Identify the blood parasite species.
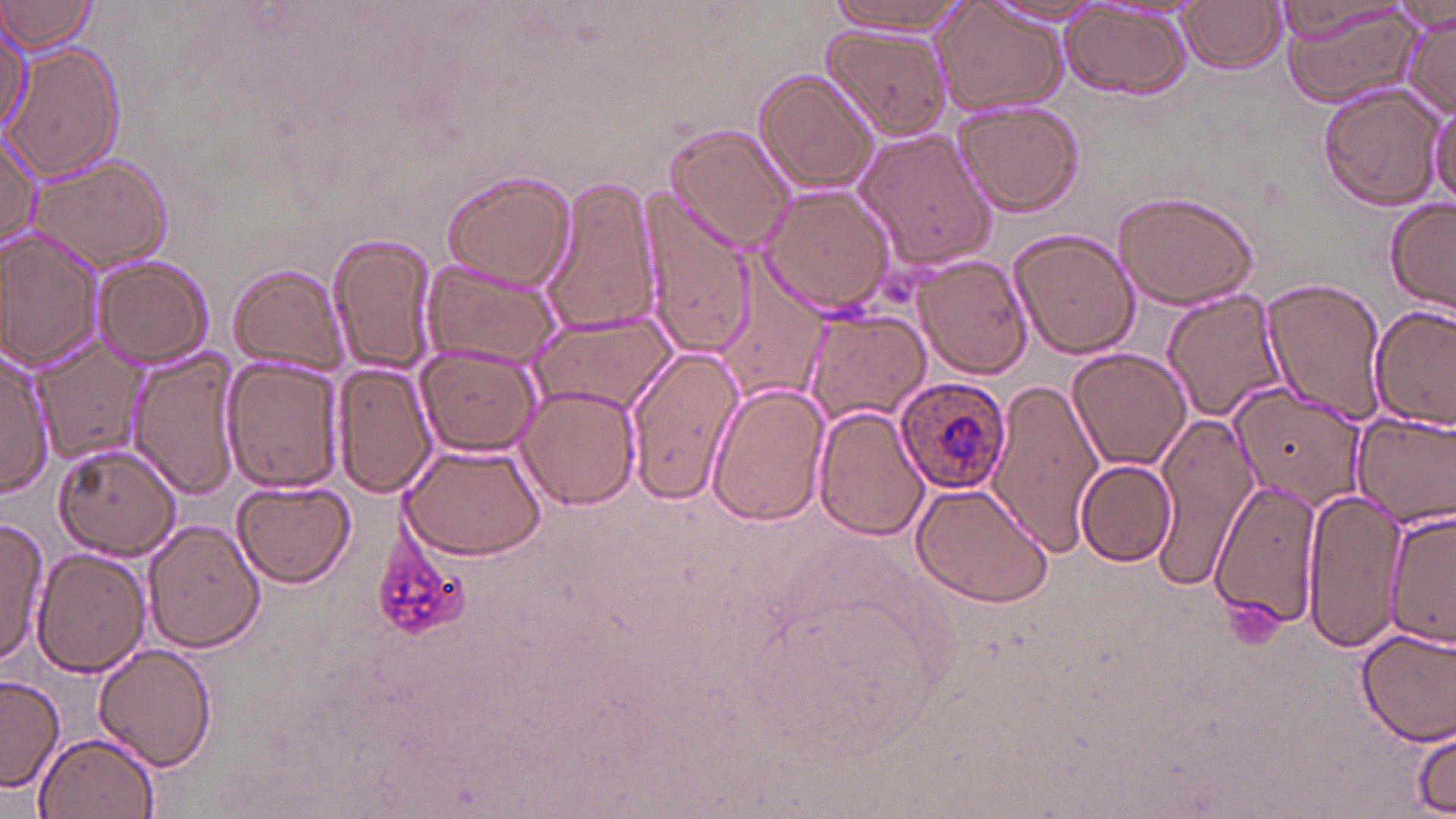

Plasmodium ovale.

magnification = 1000x
image size = 1456×819 pixels
stain = May-Grünwald-Giemsa
modality = optical microscopy
field of view = one of a larger specimen
Plasmodium ovale-infected red blood cell locations = approximate bounding boxes as [x1, y1, x2, y2] in pixels: [896, 375, 1011, 496]
platelet locations = approximate bounding boxes as [x1, y1, x2, y2] in pixels: [373, 520, 474, 642], [1225, 593, 1285, 649]
preparation = thin blood film
uninfected red blood cell locations = approximate bounding boxes as [x1, y1, x2, y2] in pixels: [0, 0, 102, 58], [828, 0, 974, 35], [983, 1, 1109, 28], [1179, 1, 1287, 73], [1278, 1, 1426, 112], [933, 3, 1069, 116], [1270, 3, 1417, 45], [1060, 5, 1193, 101], [1400, 9, 1455, 121], [0, 18, 28, 137], [826, 26, 950, 144], [8, 44, 124, 182], [753, 68, 878, 195], [1321, 84, 1445, 209], [1427, 91, 1454, 213], [952, 100, 1086, 217], [1, 122, 44, 252], [666, 123, 796, 250], [855, 129, 999, 272], [29, 153, 174, 273], [440, 168, 577, 292], [539, 174, 661, 335], [760, 185, 897, 316], [641, 188, 755, 360], [1111, 189, 1261, 311], [1383, 198, 1456, 313], [1008, 227, 1140, 358], [2, 229, 104, 374], [327, 233, 440, 377], [917, 253, 1034, 379], [92, 256, 214, 367], [419, 258, 564, 372], [229, 262, 350, 376], [715, 269, 833, 402], [1260, 278, 1388, 424], [1162, 289, 1289, 420], [1370, 306, 1455, 428], [797, 308, 930, 430], [527, 309, 676, 416], [32, 336, 144, 465], [415, 344, 542, 456], [623, 346, 745, 505], [1067, 347, 1192, 472], [126, 348, 242, 499], [0, 349, 53, 497], [220, 353, 345, 495], [334, 360, 437, 499], [1227, 379, 1374, 509], [988, 380, 1102, 556], [708, 382, 831, 526], [516, 383, 641, 510], [812, 402, 931, 542], [1151, 409, 1262, 592], [1350, 409, 1456, 528], [400, 443, 548, 561], [52, 445, 181, 559], [1075, 459, 1179, 567], [231, 479, 355, 589], [1211, 479, 1323, 628], [910, 481, 1055, 609], [1302, 490, 1410, 655], [1382, 504, 1454, 651], [143, 518, 267, 653], [0, 519, 46, 670], [31, 548, 150, 678], [1356, 627, 1456, 746], [92, 643, 216, 773], [1, 672, 66, 793], [1410, 727, 1454, 814], [34, 729, 161, 819]